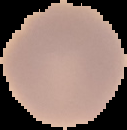

Summary:
  - Preparation: thin blood film
  - Image type: segmented cell region on a black background
  - Result: negative for Plasmodium parasites
  - Image size: 127×130 pixels